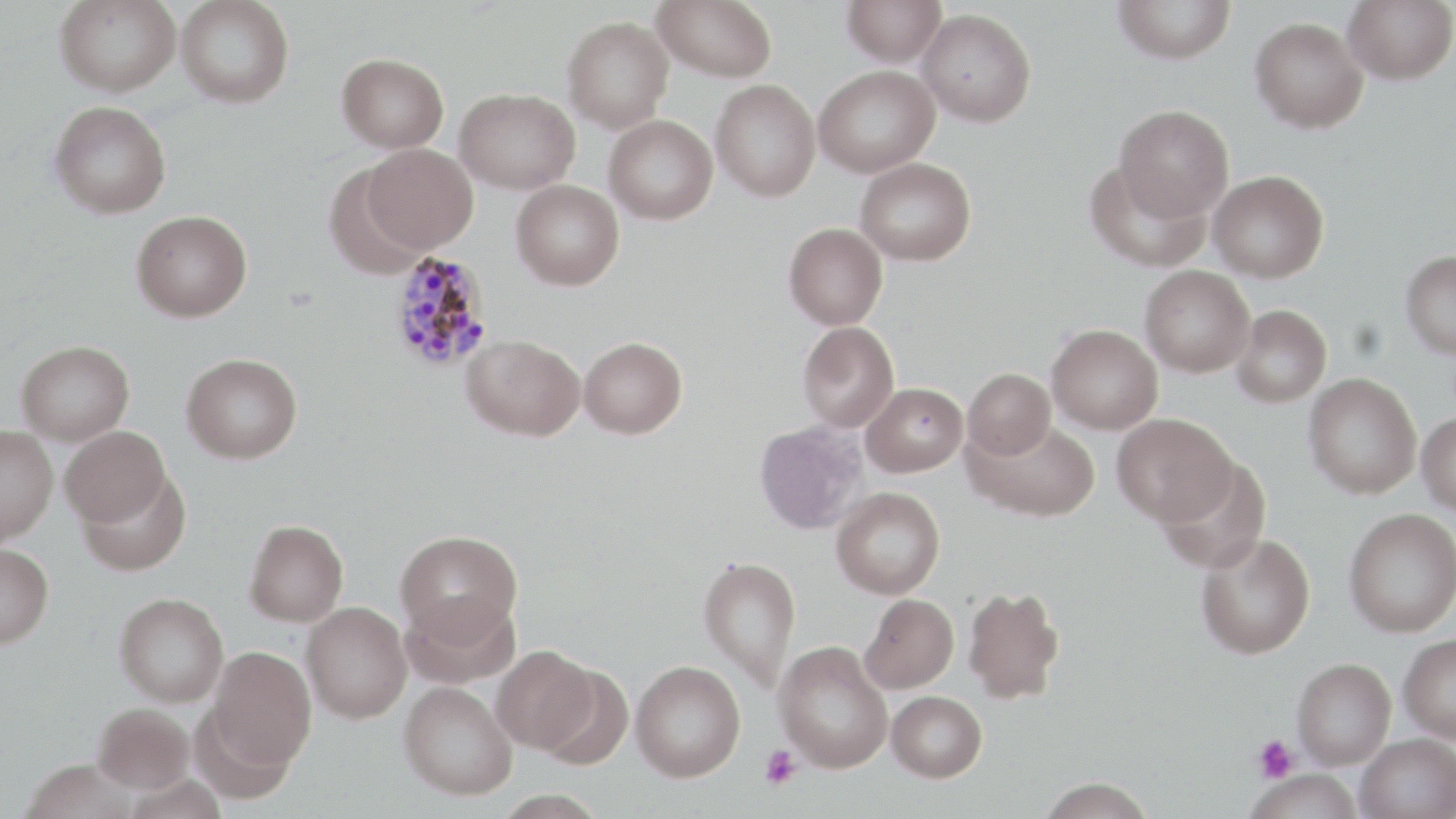 Approximate bounding boxes as (x1, y1, x2, y2) in pixels. Platelet locations: (1253, 735, 1298, 783), (760, 746, 801, 789). Plasmodium malariae-infected red blood cell locations: (390, 251, 495, 372). Uninfected red blood cell locations: (54, 0, 181, 97), (176, 0, 294, 108), (653, 0, 778, 82), (842, 0, 946, 67), (1113, 0, 1236, 65), (1342, 0, 1456, 84), (917, 8, 1037, 127), (562, 15, 674, 133), (1249, 16, 1368, 133), (337, 52, 449, 152), (813, 65, 940, 178), (710, 79, 821, 202), (455, 87, 580, 194), (49, 101, 171, 219), (1114, 104, 1234, 221), (603, 114, 718, 225), (363, 143, 478, 253), (855, 157, 976, 266), (1086, 160, 1209, 272), (323, 163, 427, 280), (1209, 170, 1328, 282), (511, 179, 624, 290), (131, 210, 252, 322), (784, 222, 888, 330), (1400, 250, 1456, 358), (1139, 265, 1255, 377), (1232, 304, 1332, 407), (798, 321, 899, 432), (1047, 323, 1163, 434), (461, 333, 585, 441), (579, 336, 687, 438), (17, 340, 134, 445), (181, 352, 303, 464), (963, 368, 1055, 459), (1303, 372, 1422, 499), (861, 382, 968, 476), (1417, 412, 1456, 515), (1112, 413, 1236, 525), (966, 418, 1099, 522), (754, 421, 868, 534), (0, 425, 58, 546), (60, 426, 170, 527), (1157, 457, 1271, 573), (76, 469, 191, 576), (831, 486, 945, 599), (1344, 508, 1456, 637), (244, 520, 349, 626), (396, 530, 522, 642), (1195, 533, 1315, 659), (0, 544, 53, 648), (698, 555, 802, 691), (963, 585, 1065, 704), (400, 591, 521, 689), (114, 592, 229, 706), (859, 593, 959, 693), (302, 602, 412, 723), (1398, 634, 1456, 742), (773, 641, 893, 772), (491, 645, 597, 753), (206, 646, 316, 769), (1291, 658, 1396, 768), (631, 660, 745, 782), (534, 662, 634, 771), (399, 681, 517, 800), (887, 690, 987, 782), (93, 703, 194, 793), (1356, 733, 1456, 819), (21, 761, 137, 819), (1247, 768, 1365, 819), (1036, 777, 1156, 819). Slide-level diagnosis: Plasmodium malariae. May-Grünwald-Giemsa stain. Image is 1456×819 pixels. Light microscopy. One field of a larger specimen. Thin blood film. 1000x magnification.